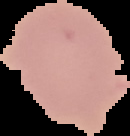
Segmented cell region on a black background. From a thin blood smear. Result: no Plasmodium parasites seen. Image is 130×136 pixels.